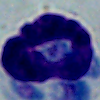

Summary:
  - Modality: photomicrograph
  - Magnification: 1000x
  - Identification: white blood cell